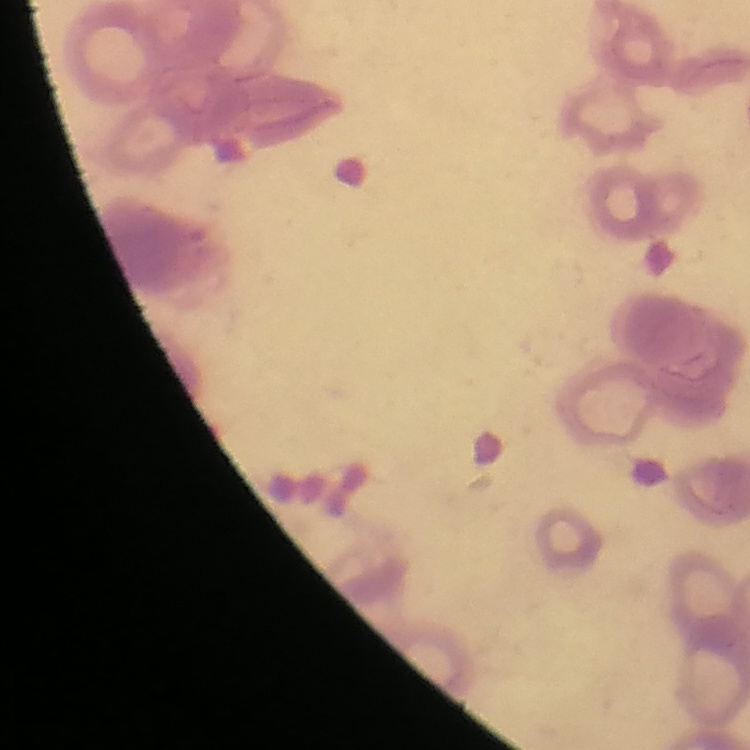

Summary:
  - Erythrocyte morphology: rouleaux formation
  - Preparation: thin peripheral smear
  - Stain: Field's or Giemsa
  - Image type: one tile cut from a larger photomicrograph